Classify this cell by malaria status.
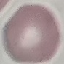

Uninfected.

Thin blood film. Automatically extracted cell patch, resized to 64 × 64 pixels. Giemsa stain. Acquired by smartphone through the microscope eyepiece.